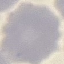

malaria status = uninfected
stain = Giemsa
preparation = thin blood film
capture = smartphone camera at the microscope eyepiece
image type = automatically extracted cell patch, resized to 64 × 64 pixels